Assess this cell for malaria.
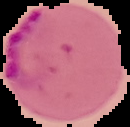
Parasitized.

Summary:
  - Image size: 130×127 pixels
  - Preparation: thin blood film
  - Image type: segmented cell region with the area outside set to black